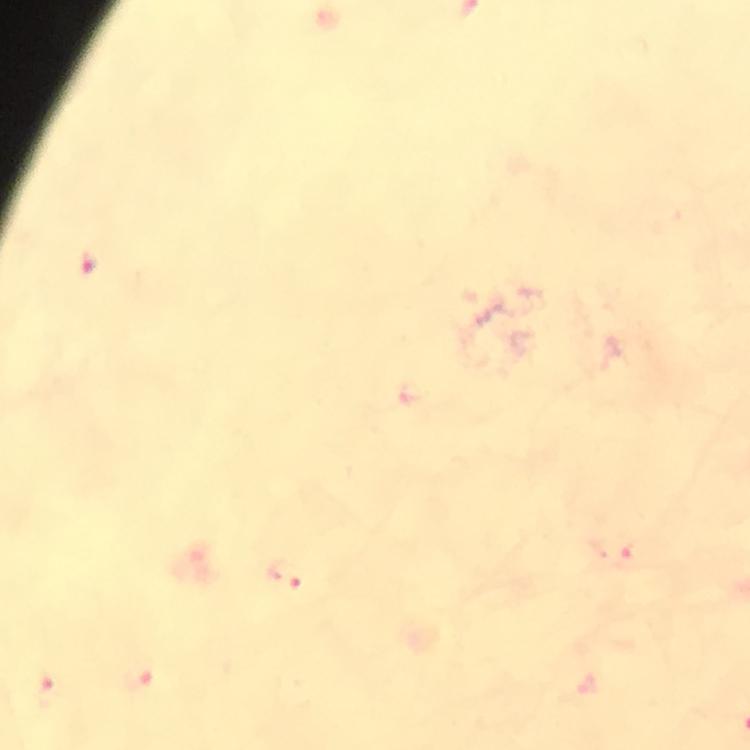
Approximate centers as {x, y} in pixels.
Summary:
  - Malaria parasite locations: {89, 264}, {612, 550}, {285, 574}, {138, 676}, {46, 689}
  - Image size: 750×750 pixels
  - Magnification: 100x
  - Context: from a diagnostic examination for malaria
  - Capture: smartphone camera through the microscope
  - Immersion oil: used
  - Preparation: thick smear
  - Stain: Giemsa
  - Cropped from: a single field of view